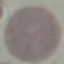
malaria status = uninfected
image type = automatically extracted cell patch, resized to 64 × 64 pixels
preparation = thin smear
stain = Giemsa
capture = smartphone through the microscope eyepiece